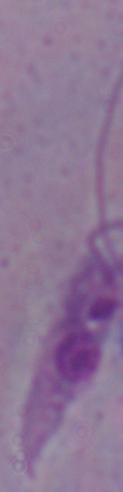 A Leishmania parasite is shown. Micrograph. 1000x magnification.